Give the position of every leukocyte visible.
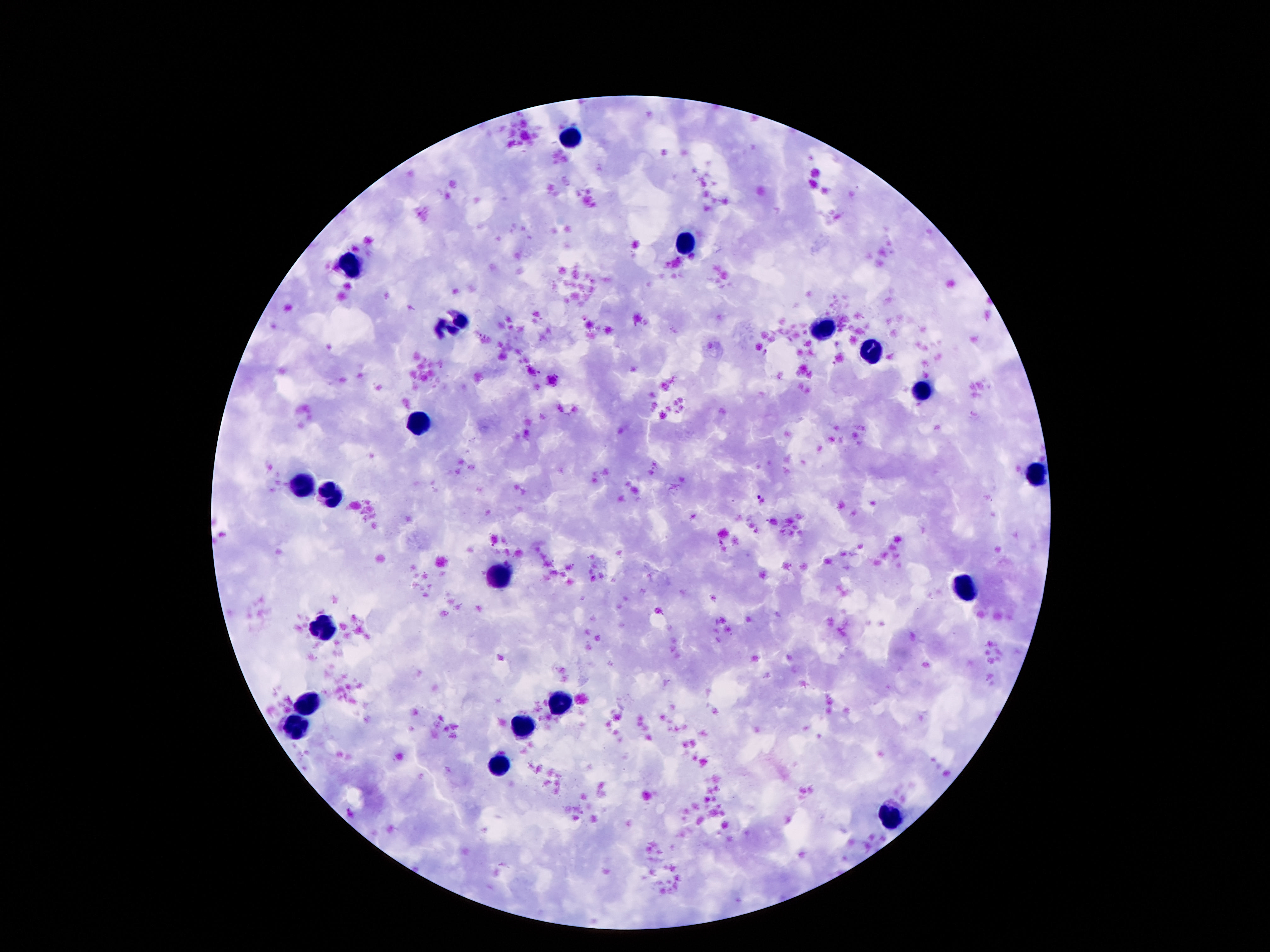

Approximate centers as [x, y] in pixels.
Leukocytes: [569, 137], [687, 245], [353, 267], [452, 323], [823, 330], [872, 353], [922, 392], [420, 422], [1038, 474], [299, 488], [330, 495], [500, 577], [965, 590], [323, 626], [308, 705], [562, 705], [295, 728], [525, 728], [500, 764], [891, 821].

image size = 1270×952 pixels
stain = Giemsa
capture = smartphone camera through the microscope eyepiece
preparation = thick peripheral-blood smear
patient malaria status = uninfected
field of view = one from this slide
magnification = 100x